State which parasite is depicted.
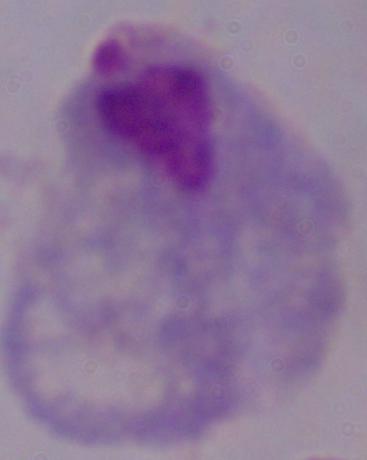

This is a trichomonad.

Summary:
  - Modality: micrograph
  - Magnification: 1000x